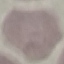
result = no malaria parasites seen
stain = Giemsa
capture = smartphone camera at the microscope eyepiece
preparation = thin blood smear
image type = cell patch, automatically extracted from a larger field of view and resized to 64 × 64 pixels